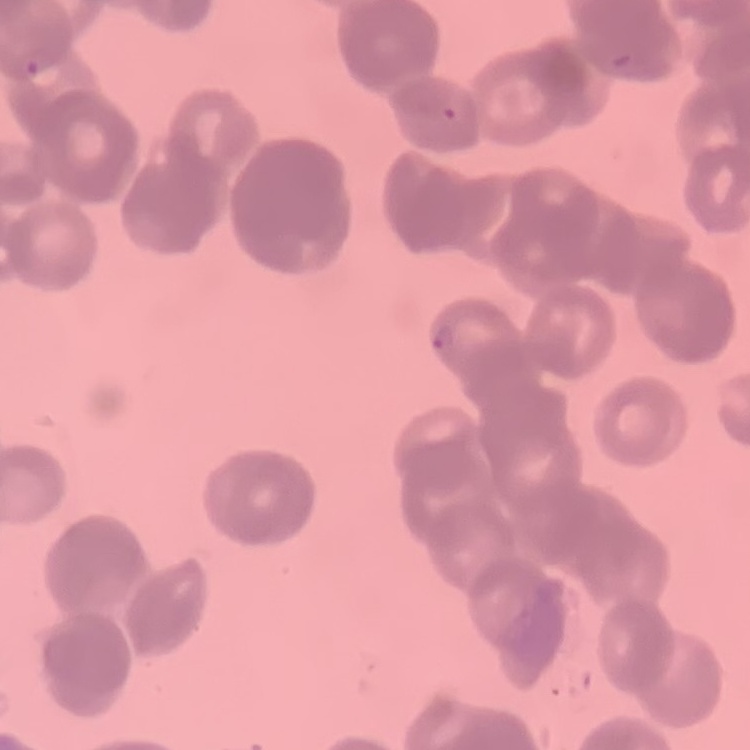

red_blood_cell_morphology: rouleaux formation
preparation: thin blood film
stain: Field's or Giemsa
image_type: one tile cut from a larger photomicrograph